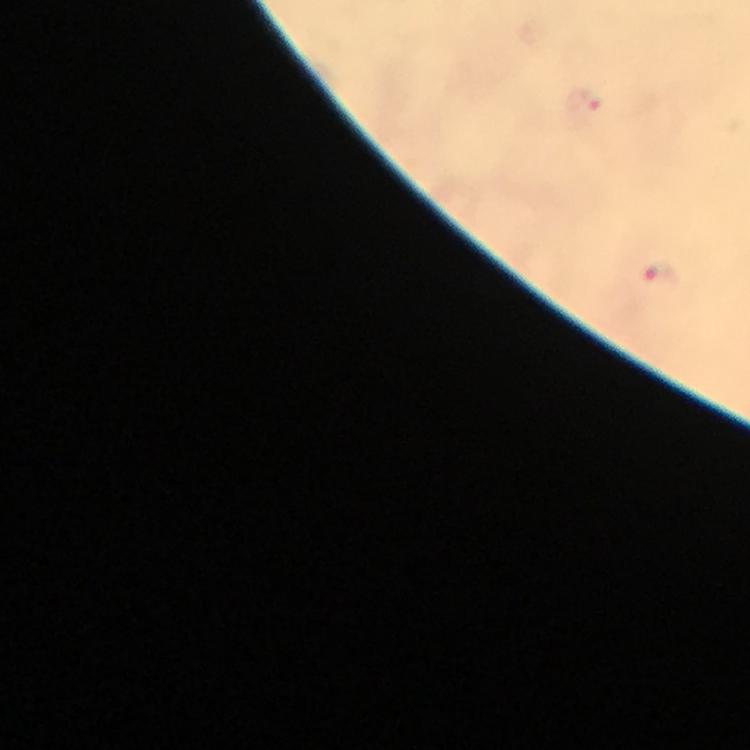
context = from a malaria diagnostic workup
capture = smartphone photograph through a microscope
image size = 750×750 pixels
cropped from = one field of view
stain = Giemsa
immersion oil = applied
Plasmodium parasite locations = approximate object centers, in pixels from the top-left corner: (x=585, y=101), (x=663, y=276)
preparation = thick blood smear
magnification = 100x